Report the malaria status of this cell.
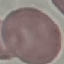
It is uninfected.

{
  "preparation": "thin blood film",
  "capture": "smartphone through the microscope eyepiece",
  "stain": "Giemsa",
  "image_type": "cell patch, automatically extracted from a larger field of view and resized to 64 × 64 pixels"
}